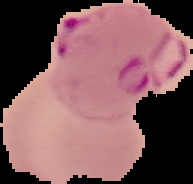
Summary:
  - Image size: 193×184 pixels
  - Preparation: thin blood film
  - Result: Plasmodium parasites identified
  - Image type: segmented cell region with the area outside set to black